Report the malaria status of this cell.
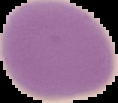

Uninfected.

Summary:
  - Preparation: thin blood film
  - Image size: 118×103 pixels
  - Image type: cell region segmented out of the field of view; surrounding area masked to black